Name the cell type shown.
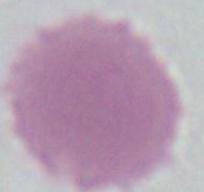
This is an erythrocyte.

Summary:
  - Modality: micrograph
  - Magnification: 1000x